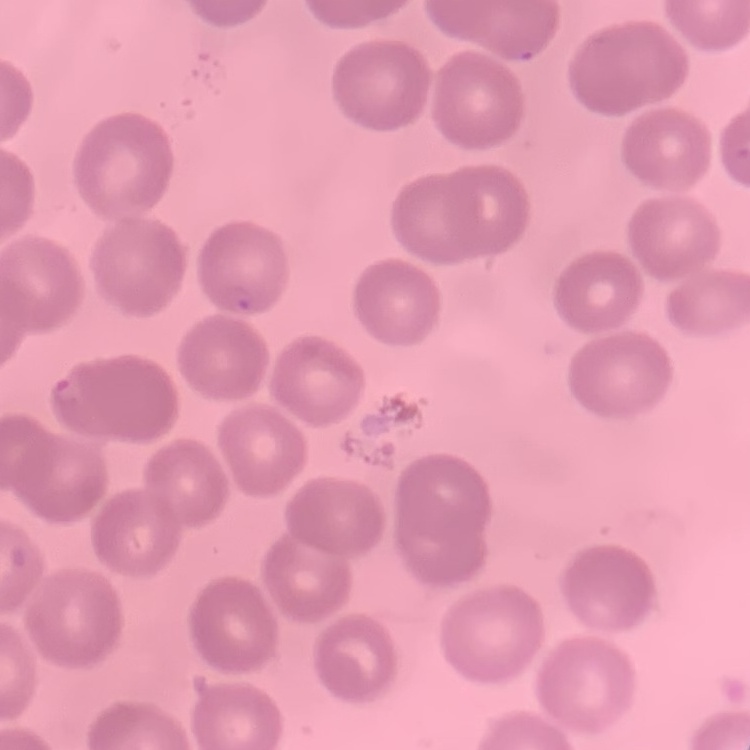
Summary:
  - Red blood cell morphology: no rouleaux formation
  - Image type: square crop of a larger photomicrograph
  - Stain: Field's or Giemsa
  - Preparation: thin blood film